Comment on the morphology of the red blood cells.
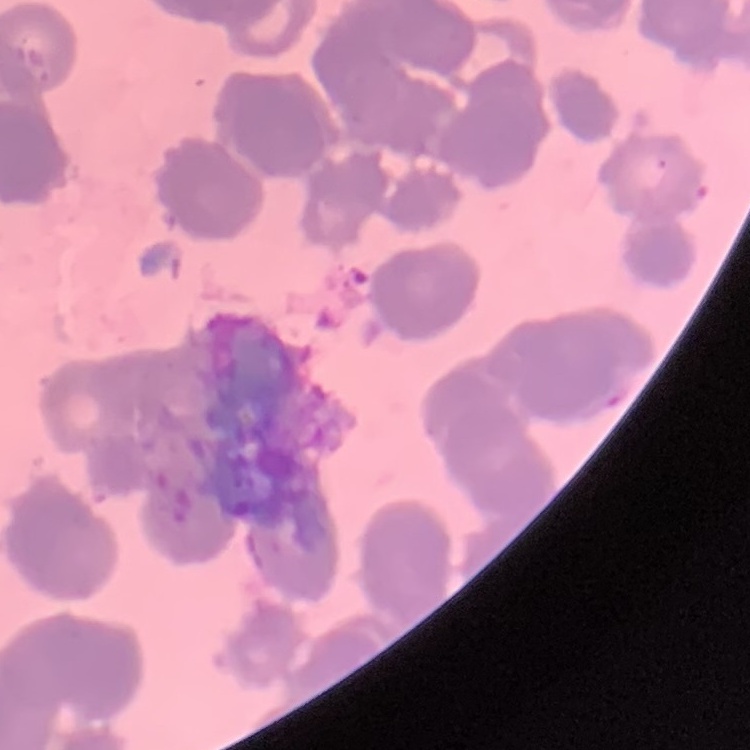

They show rouleaux formation.

preparation = thin peripheral smear
image type = square crop of a larger photomicrograph
stain = Field's or Giemsa